Identify the preparation type.
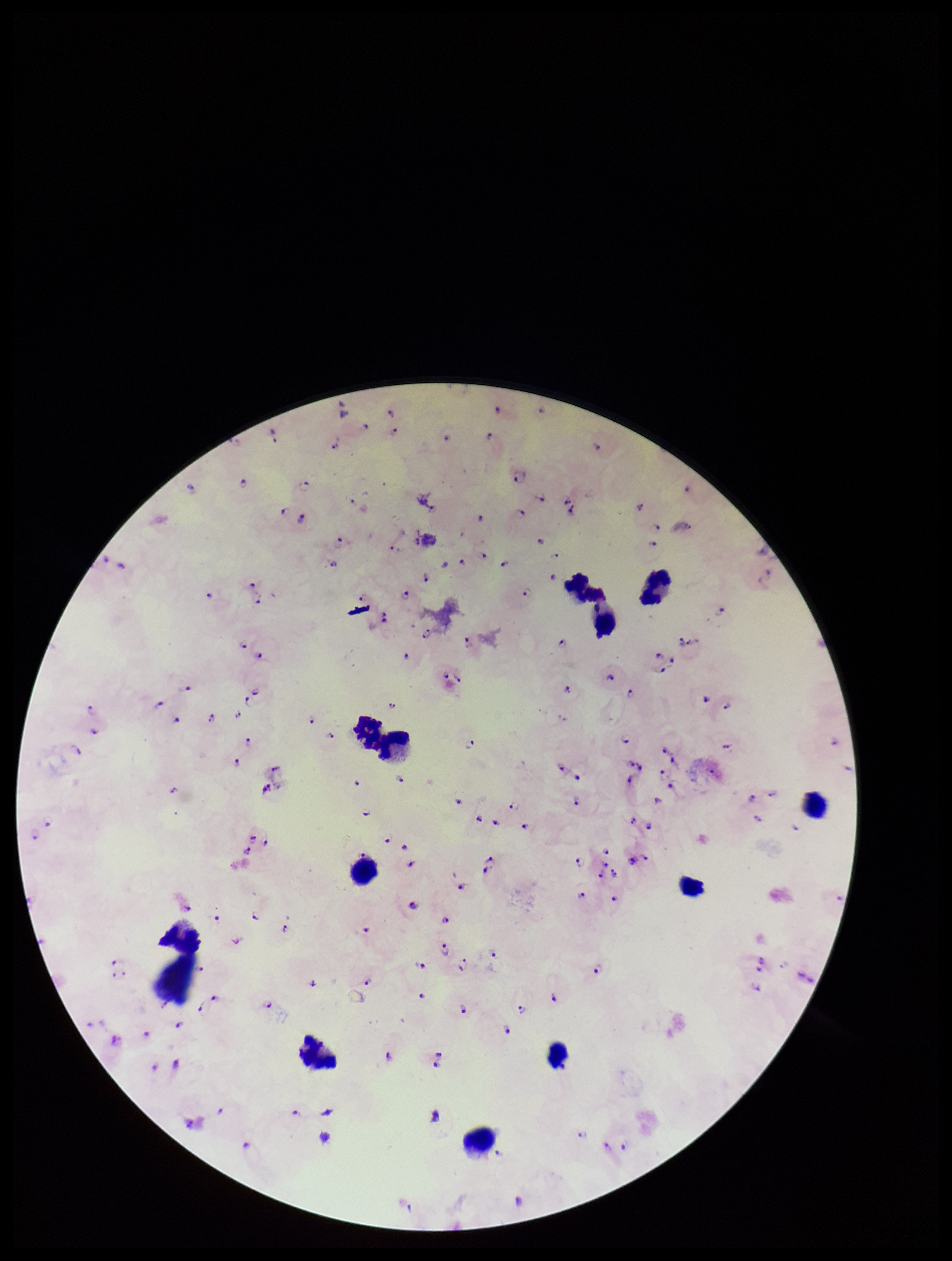
Thick.

patient_malaria_status: infected
capture: smartphone photograph through the microscope eyepiece
species_reported_for_this_patient: Plasmodium falciparum
image_size: 952×1261 pixels
plasmodium_parasites: seen
field_of_view: single
leukocyte_count: 11
parasite_count: 120
stain: Giemsa